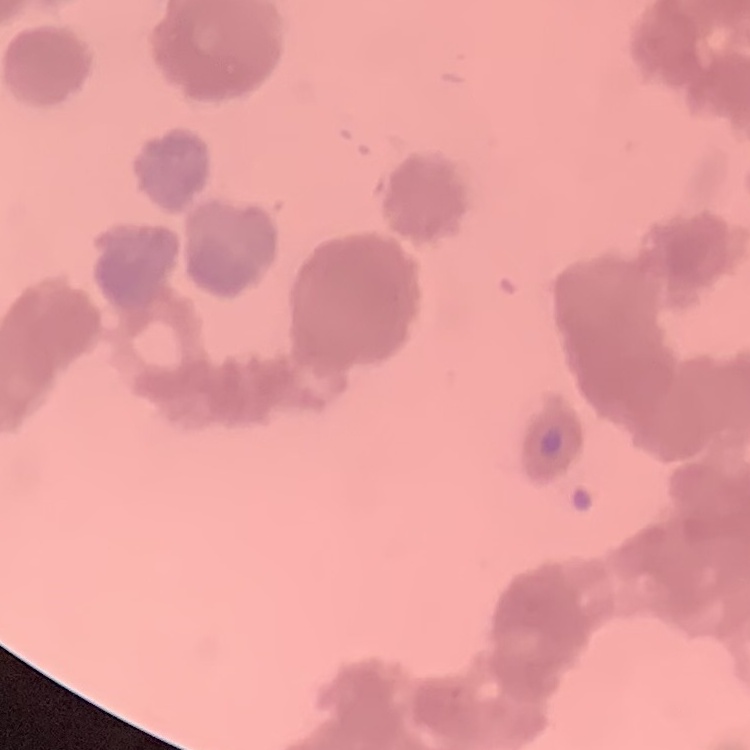
Summary:
  - Erythrocyte morphology: rouleaux formation
  - Image type: one tile cut from a larger photomicrograph
  - Preparation: thin peripheral smear
  - Stain: Field's or Giemsa